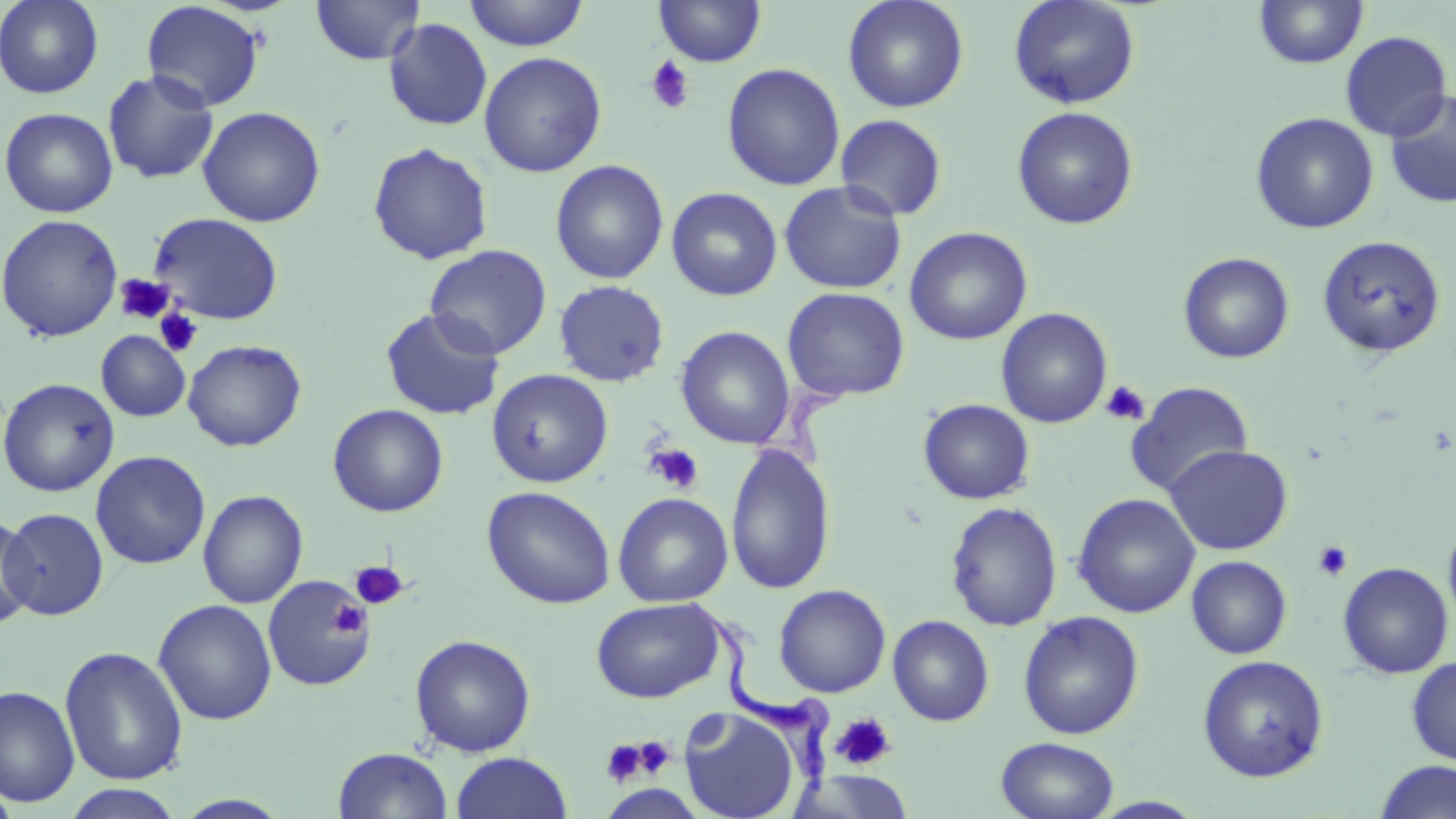
Summary:
  - Coordinate format: approximate bounding boxes as (x1, y1, x2, y2) in pixels
  - Trypanosoma brucei locations: (684, 597, 832, 797)
  - Platelet locations (subset): (645, 55, 695, 114), (114, 274, 174, 324), (154, 308, 205, 358), (1101, 380, 1150, 426), (644, 443, 704, 494), (1312, 540, 1353, 582), (350, 561, 408, 610), (329, 601, 369, 638), (831, 712, 896, 771), (630, 736, 676, 779), (601, 739, 649, 788)
  - Uninfected red blood cell locations (subset): (0, 0, 104, 99), (311, 0, 426, 65), (462, 0, 589, 51), (653, 0, 767, 67), (842, 0, 969, 113), (1008, 0, 1140, 110), (141, 1, 265, 112), (1254, 1, 1369, 69), (383, 18, 493, 131), (1340, 30, 1453, 141), (479, 51, 607, 177), (721, 63, 846, 191), (102, 69, 219, 184), (1384, 90, 1456, 209), (197, 106, 326, 227), (1011, 106, 1139, 230), (1, 107, 118, 218), (1250, 112, 1379, 234), (835, 114, 948, 221), (367, 142, 494, 265), (550, 159, 669, 284), (779, 180, 907, 295), (666, 186, 783, 301), (148, 212, 284, 325), (0, 213, 123, 342), (904, 226, 1033, 345), (1317, 235, 1446, 359), (424, 244, 552, 359), (1177, 251, 1295, 364), (553, 280, 670, 387), (781, 287, 910, 402), (996, 307, 1113, 428), (380, 308, 506, 420), (675, 325, 796, 450), (96, 330, 190, 421), (182, 339, 306, 452), (486, 368, 613, 488), (0, 377, 120, 497), (1126, 381, 1254, 496), (918, 398, 1035, 505), (327, 403, 448, 517), (725, 443, 836, 595), (1164, 444, 1293, 555), (90, 451, 211, 569), (481, 485, 617, 609), (197, 489, 308, 608), (612, 492, 733, 607), (1072, 493, 1200, 618), (945, 501, 1063, 631), (1, 507, 109, 620), (1442, 510, 1456, 637), (0, 512, 36, 631), (1186, 555, 1292, 659), (1337, 562, 1453, 678), (773, 584, 891, 698), (591, 597, 725, 703), (153, 599, 277, 725), (1017, 610, 1144, 740), (887, 615, 995, 726), (409, 633, 537, 757), (59, 646, 188, 786), (1197, 654, 1329, 783), (1407, 656, 1456, 766), (1, 684, 80, 808), (679, 707, 801, 819), (996, 736, 1120, 819), (332, 747, 453, 819), (450, 751, 573, 819), (1374, 759, 1456, 819), (0, 779, 19, 819), (59, 784, 187, 819)
  - Slide-level diagnosis: Trypanosoma brucei
  - Stain: May-Grünwald-Giemsa
  - Modality: light microscopy
  - Preparation: thin blood film
  - Magnification: 1000x
  - Field of view: one of a larger specimen
  - Image size: 1456×819 pixels